Classify this cell by malaria status.
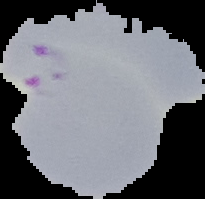

Parasitized.

From a thin blood film. Image is 205×199 pixels. The area outside the segmented cell region is set to black.